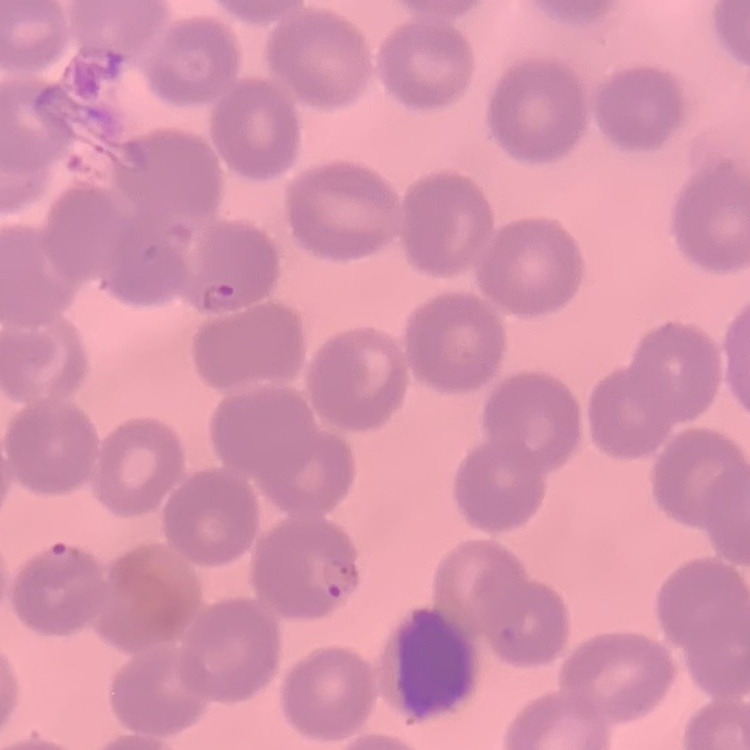

erythrocyte morphology = no rouleaux formation
stain = Field's or Giemsa
image type = square crop of a larger photomicrograph
preparation = thin blood smear